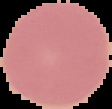
image type = segmented cell region with the area outside set to black
malaria status = uninfected
preparation = thin blood smear
image size = 112×109 pixels